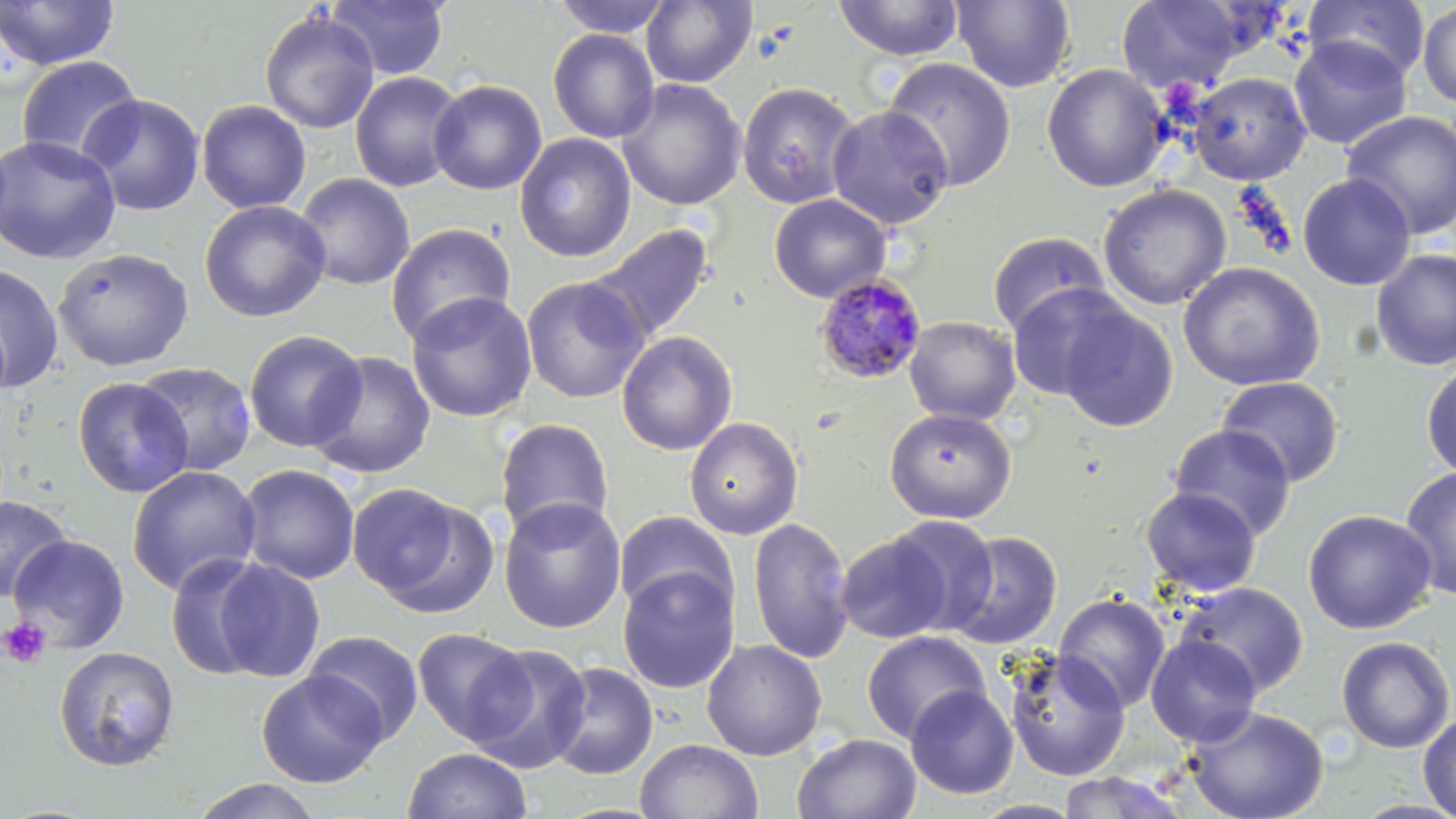
Approximate bounding boxes as (x1, y1, x2, y2) in pixels. Uninfected red blood cell locations: (0, 0, 119, 71), (551, 0, 674, 38), (641, 0, 757, 88), (833, 0, 965, 61), (951, 0, 1076, 93), (1116, 0, 1249, 94), (1304, 0, 1430, 85), (327, 1, 450, 81), (1417, 2, 1456, 109), (259, 9, 380, 134), (548, 28, 659, 143), (1289, 35, 1412, 150), (16, 55, 143, 165), (881, 57, 1017, 192), (1042, 64, 1170, 192), (349, 71, 465, 192), (1187, 72, 1311, 185), (428, 79, 547, 195), (617, 79, 746, 210), (736, 81, 861, 209), (79, 93, 205, 217), (196, 100, 311, 213), (827, 105, 953, 229), (1342, 110, 1456, 239), (515, 133, 636, 262), (0, 134, 122, 265), (294, 172, 415, 291), (1297, 173, 1416, 291), (1098, 183, 1232, 310), (769, 194, 891, 303), (200, 200, 331, 322), (585, 222, 716, 346), (385, 223, 516, 348), (987, 230, 1110, 337), (53, 247, 194, 372), (1371, 249, 1456, 372), (1178, 261, 1325, 391), (0, 263, 64, 393), (520, 276, 649, 404), (1006, 282, 1131, 402), (406, 291, 537, 423), (1056, 303, 1179, 433), (904, 316, 1021, 425), (243, 330, 367, 453), (616, 330, 737, 456), (306, 350, 436, 479), (133, 362, 258, 478), (1421, 362, 1456, 479), (1216, 376, 1345, 487), (73, 377, 194, 498), (884, 408, 1017, 523), (683, 416, 803, 540), (494, 418, 615, 541), (1168, 424, 1296, 541), (236, 464, 360, 585), (127, 465, 261, 596), (1400, 467, 1456, 600), (346, 483, 480, 609), (1140, 487, 1262, 596), (0, 496, 73, 602), (498, 496, 627, 634), (1303, 508, 1437, 635), (613, 510, 738, 619), (886, 515, 999, 634), (748, 516, 853, 664), (945, 531, 1062, 650), (835, 532, 955, 643), (8, 535, 130, 652), (165, 553, 272, 681), (212, 559, 326, 682), (617, 566, 740, 694), (1174, 582, 1309, 697), (1054, 592, 1170, 714), (412, 627, 532, 745), (304, 629, 424, 744), (861, 630, 990, 744), (1145, 634, 1261, 748), (1336, 636, 1455, 753), (701, 638, 827, 761), (465, 642, 593, 773), (53, 646, 180, 771), (1003, 649, 1130, 781), (548, 661, 658, 780), (257, 670, 386, 788), (905, 685, 1018, 799), (1185, 705, 1329, 819), (1418, 713, 1456, 819), (792, 732, 922, 819), (634, 738, 763, 819), (402, 747, 533, 819), (1056, 771, 1190, 818), (190, 778, 324, 819). Platelet locations: (1, 616, 51, 669). Plasmodium malariae-infected red blood cell locations: (813, 273, 928, 384). Slide-level diagnosis: Plasmodium malariae. Thin blood film. Light microscopy. Image is 1456×819 pixels. 1000x magnification. May-Grünwald-Giemsa-stained preparation. Single field of view.